Outline each Plasmodium malariae-infected red blood cell.
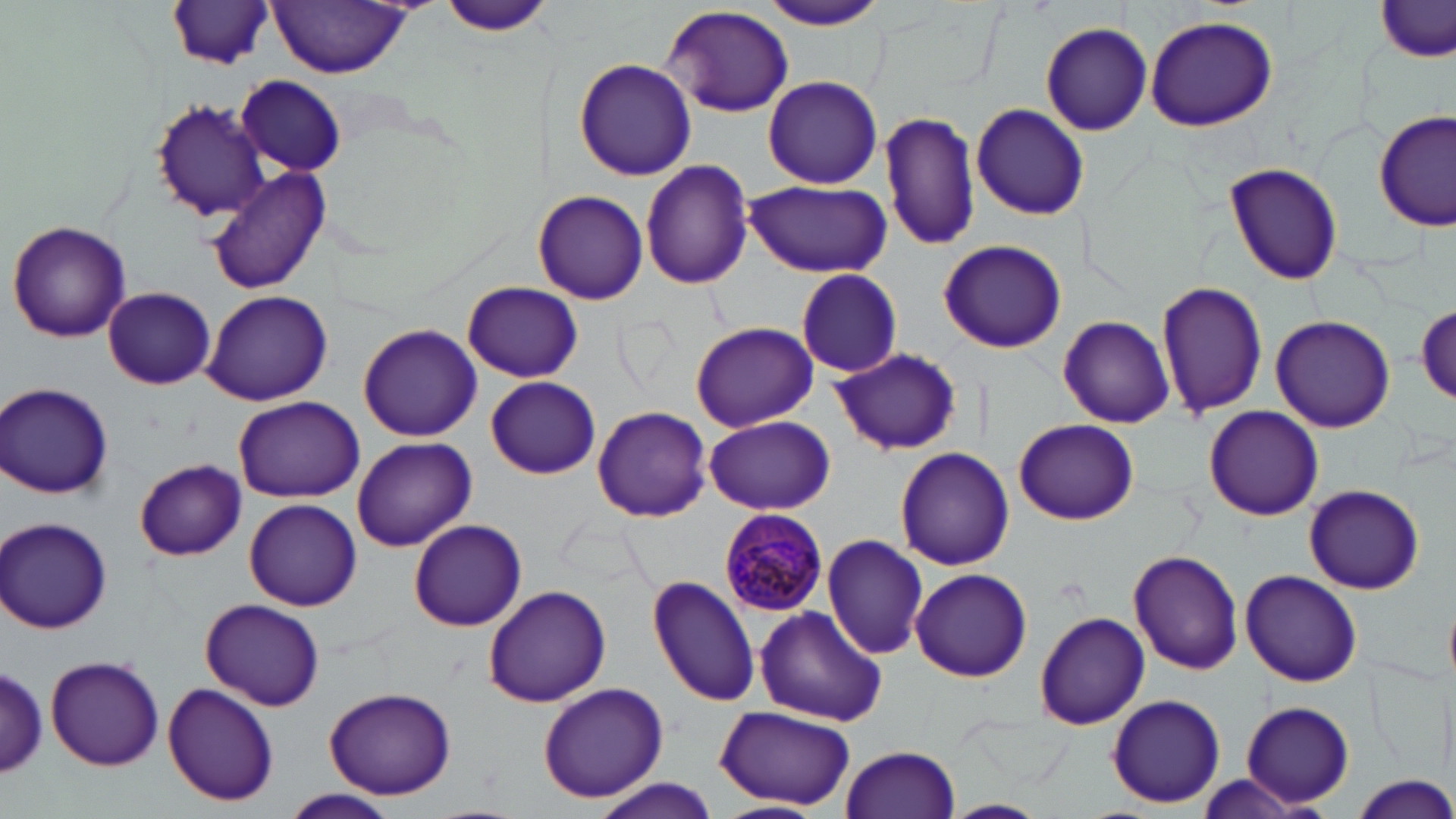

Approximate bounding boxes as named x1/y1/x2/y2 corners in pixels.
Plasmodium malariae-infected red blood cells: (x1=720, y1=508, x2=830, y2=617).

slide-level diagnosis = Plasmodium malariae
uninfected red blood cell locations = approximate bounding boxes as named x1/y1/x2/y2 corners in pixels: (x1=435, y1=0, x2=555, y2=38), (x1=760, y1=1, x2=890, y2=31), (x1=166, y1=2, x2=275, y2=71), (x1=268, y1=2, x2=415, y2=76), (x1=1376, y1=2, x2=1456, y2=65), (x1=662, y1=5, x2=795, y2=118), (x1=1144, y1=15, x2=1277, y2=131), (x1=1039, y1=22, x2=1154, y2=135), (x1=574, y1=59, x2=696, y2=180), (x1=762, y1=74, x2=883, y2=189), (x1=237, y1=76, x2=347, y2=176), (x1=150, y1=100, x2=267, y2=222), (x1=969, y1=103, x2=1091, y2=221), (x1=880, y1=109, x2=982, y2=252), (x1=1376, y1=110, x2=1453, y2=230), (x1=640, y1=160, x2=755, y2=289), (x1=1223, y1=162, x2=1344, y2=285), (x1=205, y1=167, x2=331, y2=294), (x1=743, y1=179, x2=890, y2=277), (x1=534, y1=190, x2=648, y2=305), (x1=7, y1=220, x2=131, y2=342), (x1=939, y1=240, x2=1067, y2=353), (x1=795, y1=269, x2=904, y2=378), (x1=1157, y1=278, x2=1269, y2=419), (x1=462, y1=281, x2=583, y2=382), (x1=104, y1=288, x2=216, y2=388), (x1=200, y1=289, x2=334, y2=406), (x1=1414, y1=301, x2=1456, y2=405), (x1=1057, y1=315, x2=1173, y2=428), (x1=1270, y1=316, x2=1395, y2=432), (x1=689, y1=321, x2=819, y2=431), (x1=357, y1=323, x2=483, y2=441), (x1=830, y1=347, x2=961, y2=456), (x1=486, y1=376, x2=600, y2=478), (x1=2, y1=382, x2=115, y2=499), (x1=234, y1=397, x2=367, y2=501), (x1=592, y1=405, x2=712, y2=522), (x1=1203, y1=405, x2=1323, y2=521), (x1=704, y1=415, x2=835, y2=515), (x1=1014, y1=418, x2=1138, y2=524), (x1=353, y1=436, x2=475, y2=551), (x1=894, y1=447, x2=1015, y2=571), (x1=134, y1=459, x2=247, y2=560), (x1=1305, y1=484, x2=1425, y2=594), (x1=245, y1=499, x2=361, y2=609), (x1=2, y1=517, x2=113, y2=634), (x1=409, y1=519, x2=527, y2=631), (x1=821, y1=534, x2=930, y2=659), (x1=1128, y1=549, x2=1245, y2=674), (x1=909, y1=567, x2=1032, y2=682), (x1=1240, y1=571, x2=1363, y2=687), (x1=646, y1=574, x2=761, y2=707), (x1=482, y1=584, x2=612, y2=707), (x1=200, y1=598, x2=324, y2=711), (x1=1445, y1=599, x2=1456, y2=687), (x1=753, y1=605, x2=887, y2=726), (x1=1033, y1=610, x2=1151, y2=731), (x1=45, y1=654, x2=165, y2=771), (x1=0, y1=663, x2=49, y2=782), (x1=162, y1=682, x2=280, y2=806), (x1=537, y1=682, x2=670, y2=804), (x1=323, y1=686, x2=457, y2=800), (x1=1106, y1=694, x2=1226, y2=809), (x1=1240, y1=701, x2=1353, y2=808), (x1=716, y1=704, x2=855, y2=811), (x1=841, y1=744, x2=961, y2=819), (x1=1346, y1=775, x2=1456, y2=818), (x1=590, y1=778, x2=721, y2=818), (x1=285, y1=788, x2=398, y2=818), (x1=939, y1=799, x2=1048, y2=819), (x1=716, y1=802, x2=826, y2=819)
preparation = thin blood smear
magnification = 1000x
field of view = one of a larger specimen
image size = 1456×819 pixels
stain = May-Grünwald-Giemsa
modality = light microscopy